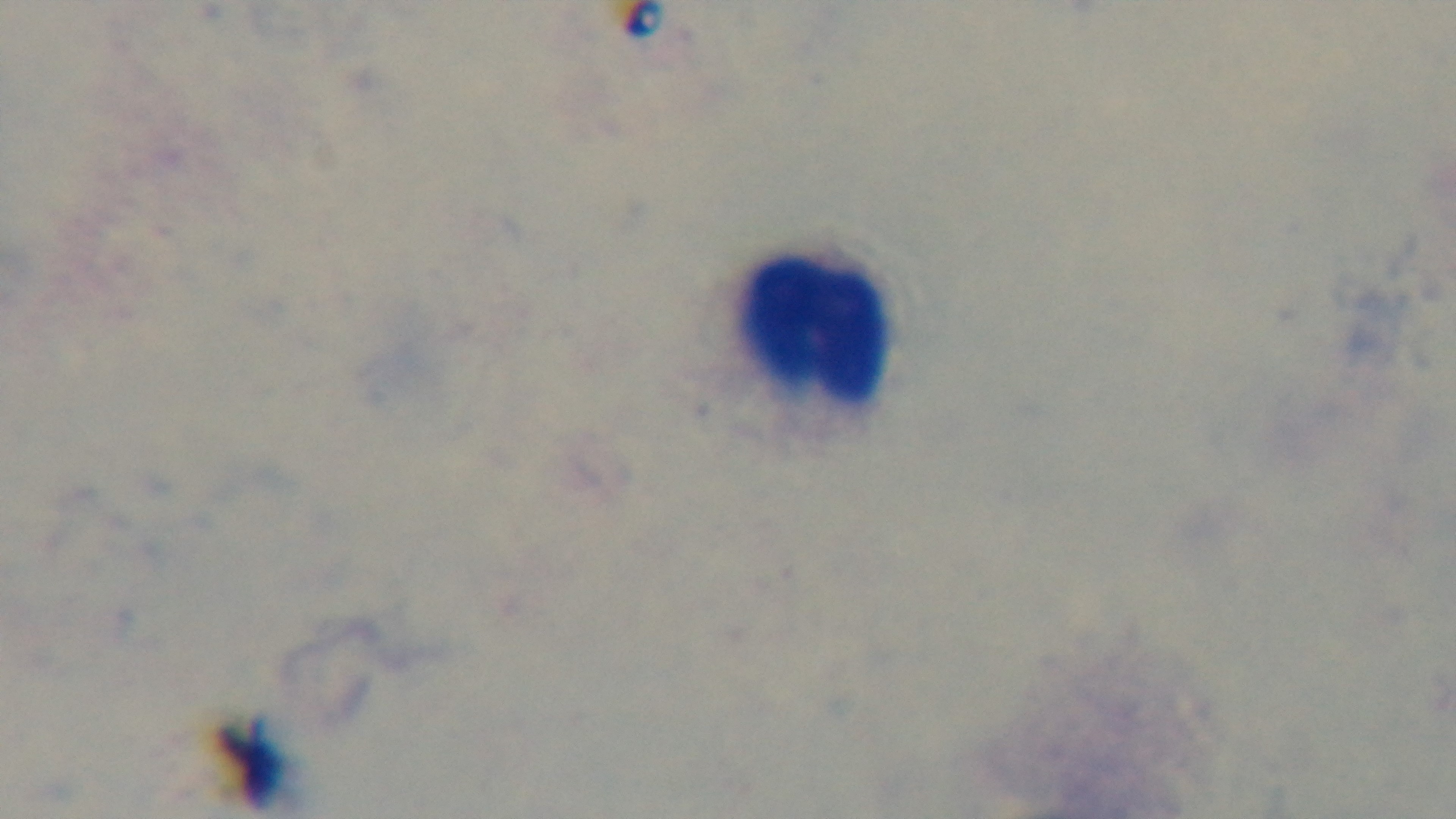
objective = 100x oil immersion
stain = Giemsa
malaria status = negative
modality = light microscopy
preparation = thick blood film
capture = mounted 4K digital camera
field of view = single